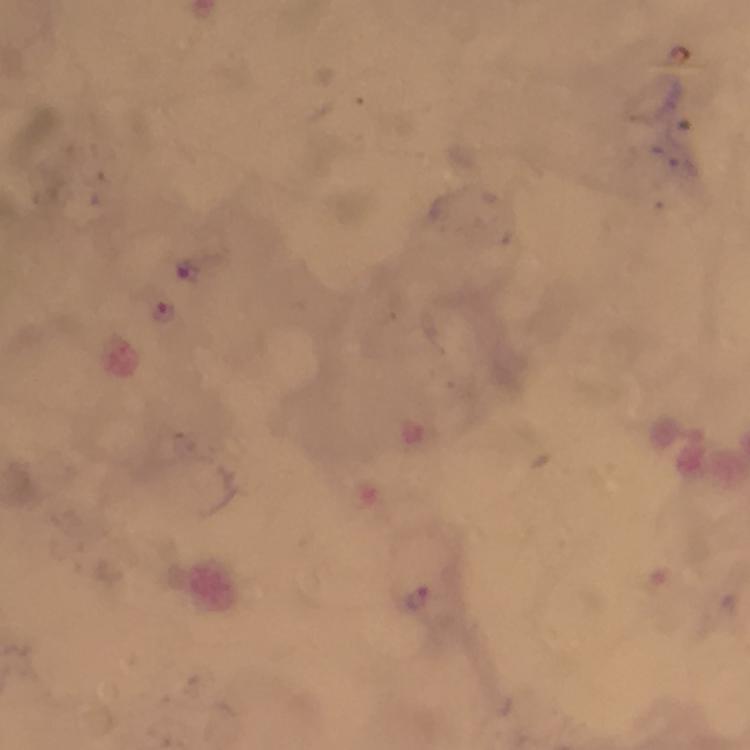

Approximate centers as [x, y] in pixels.
Summary:
  - Malaria parasite locations: [163, 313]
  - Cropped from: one field of view
  - Magnification: 100x
  - Preparation: thick blood film
  - Capture: smartphone mounted on the microscope
  - Image size: 750×750 pixels
  - Context: from a diagnostic examination for malaria
  - Immersion oil: applied
  - Stain: Giemsa